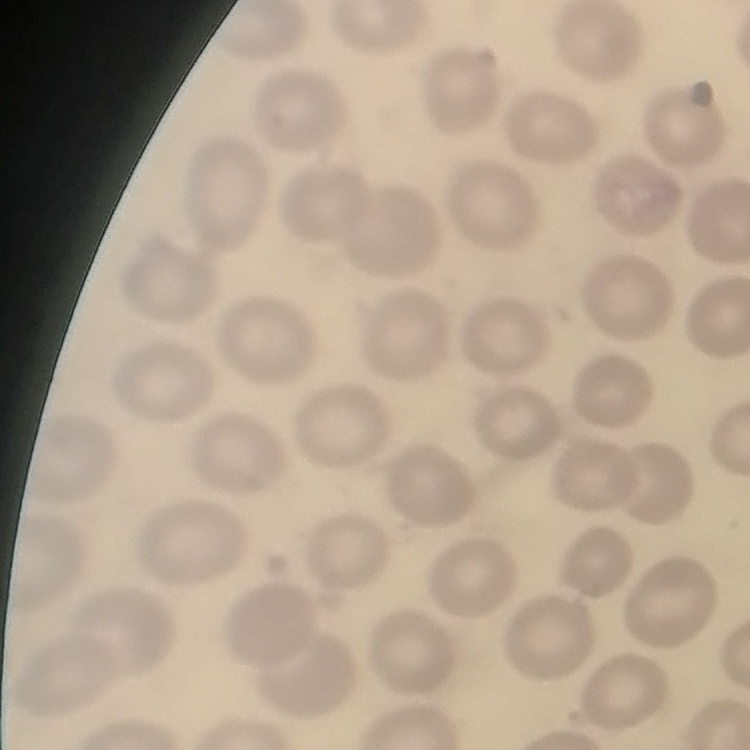
The erythrocytes exhibit no rouleaux formation. One tile cut from a larger photomicrograph. Thin blood film. Field's or Giemsa stain.